Report the malaria status of this cell.
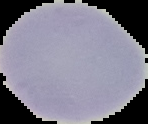
It is uninfected.

Image is 148×124 pixels. The area outside the segmented cell region is set to black. From a thin blood film.